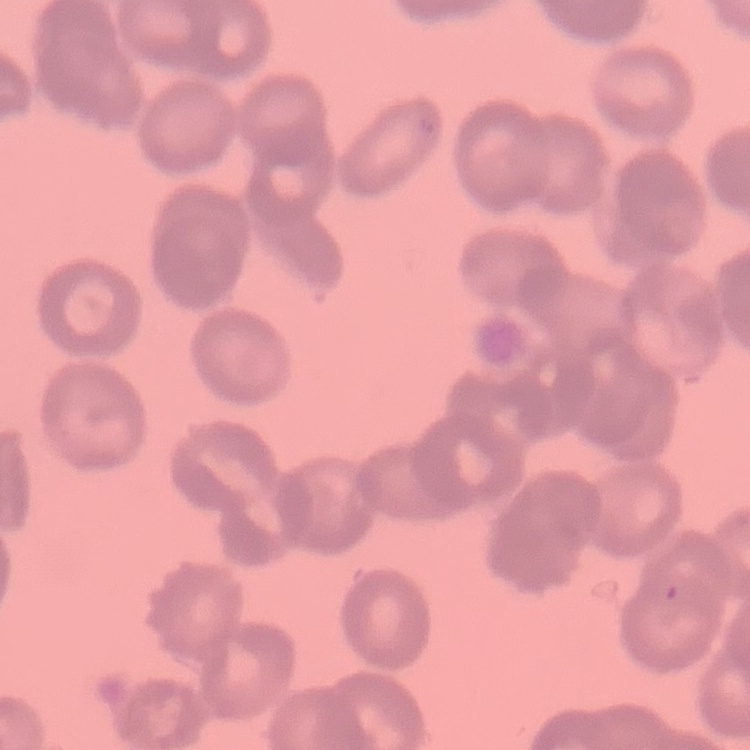

The erythrocytes show rouleaux formation. One tile cut from a larger photomicrograph. Stained with either Field's or Giemsa. Thin blood smear.